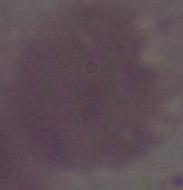
modality = micrograph
identification = red blood cell
magnification = 1000x